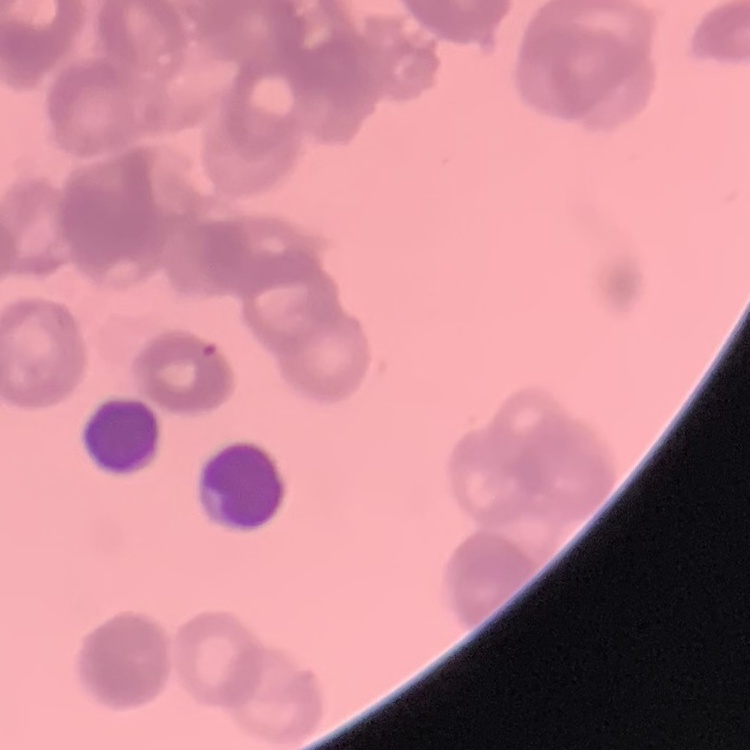
The erythrocytes show rouleaux formation. Thin peripheral smear. One tile cut from a larger photomicrograph. Stained with either Field's or Giemsa.